Locate every blood parasite and identify its species.
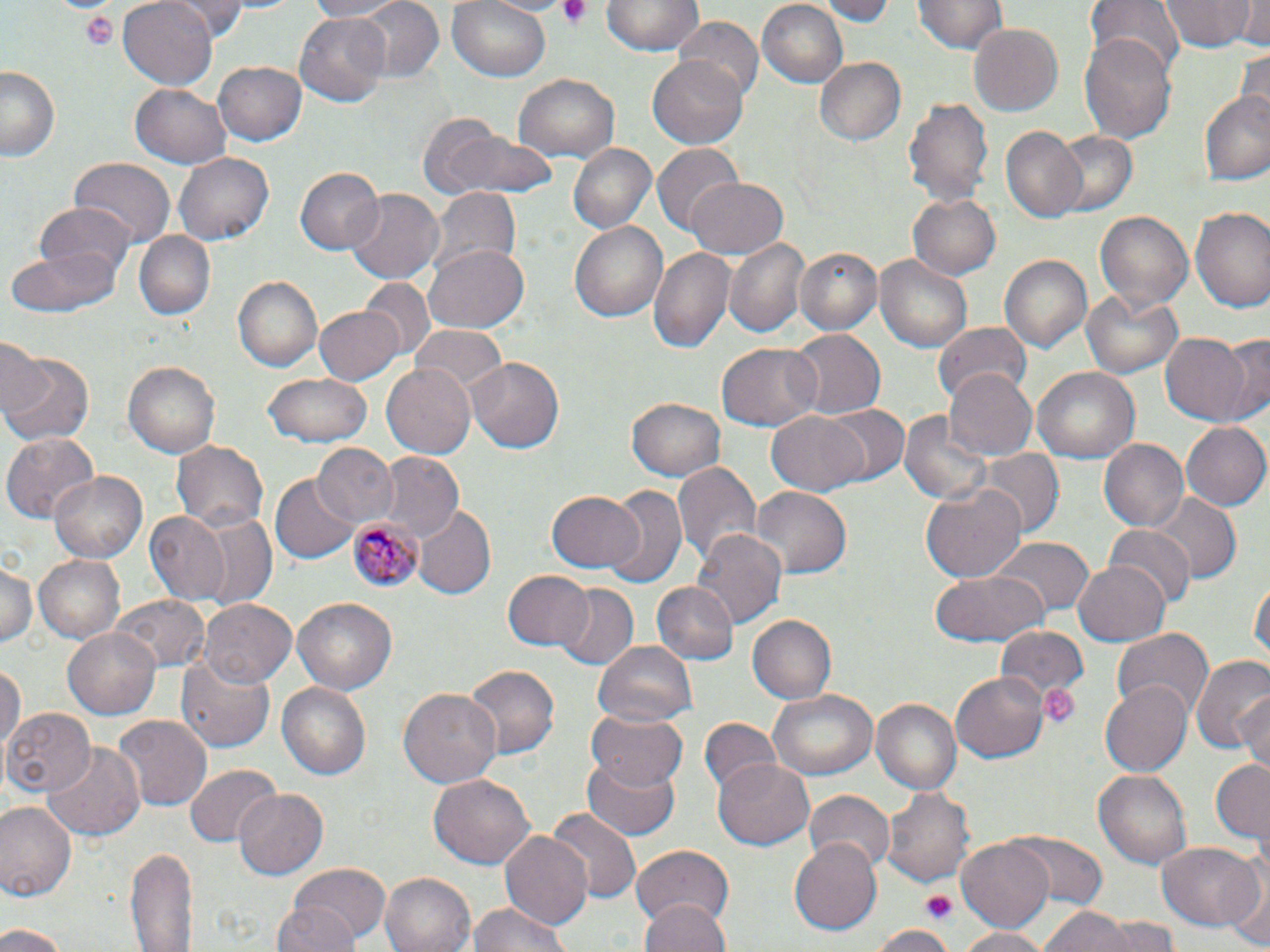

Approximate bounding boxes as named x1/y1/x2/y2 corners in pixels.
Plasmodium malariae-infected red blood cells: (x1=348, y1=516, x2=419, y2=592).
No Plasmodium falciparum, Plasmodium ovale, Plasmodium vivax, Babesia divergens, or Trypanosoma brucei observed.

{
  "slide_level_diagnosis": "Plasmodium malariae",
  "stain": "May-Grünwald-Giemsa",
  "modality": "light microscopy",
  "preparation": "thin blood film",
  "field_of_view": "single",
  "magnification": "1000x",
  "platelet_locations": "approximate bounding boxes as named x1/y1/x2/y2 corners in pixels: (x1=555, y1=0, x2=595, y2=29), (x1=79, y1=9, x2=119, y2=49), (x1=1039, y1=683, x2=1080, y2=730), (x1=920, y1=891, x2=958, y2=923)",
  "image_size": "1270×952 pixels",
  "uninfected_red_blood_cell_locations": "approximate bounding boxes as named x1/y1/x2/y2 corners in pixels: (x1=119, y1=0, x2=218, y2=89), (x1=171, y1=0, x2=256, y2=38), (x1=302, y1=0, x2=410, y2=21), (x1=346, y1=0, x2=446, y2=83), (x1=448, y1=0, x2=552, y2=82), (x1=484, y1=0, x2=573, y2=16), (x1=604, y1=0, x2=701, y2=55), (x1=815, y1=0, x2=896, y2=23), (x1=915, y1=0, x2=1006, y2=55), (x1=1085, y1=0, x2=1184, y2=79), (x1=1161, y1=0, x2=1258, y2=51), (x1=1235, y1=0, x2=1270, y2=47), (x1=755, y1=1, x2=849, y2=88), (x1=295, y1=12, x2=392, y2=106), (x1=674, y1=17, x2=763, y2=105), (x1=969, y1=22, x2=1064, y2=116), (x1=1083, y1=30, x2=1177, y2=146), (x1=1235, y1=46, x2=1270, y2=125), (x1=648, y1=55, x2=752, y2=150), (x1=813, y1=56, x2=909, y2=148), (x1=212, y1=61, x2=307, y2=146), (x1=2, y1=66, x2=62, y2=163), (x1=511, y1=74, x2=618, y2=163), (x1=131, y1=84, x2=232, y2=169), (x1=1200, y1=89, x2=1270, y2=185), (x1=903, y1=95, x2=993, y2=208), (x1=416, y1=114, x2=551, y2=202), (x1=999, y1=126, x2=1086, y2=220), (x1=1045, y1=130, x2=1138, y2=217), (x1=567, y1=142, x2=656, y2=233), (x1=651, y1=144, x2=743, y2=234), (x1=175, y1=152, x2=272, y2=245), (x1=70, y1=160, x2=174, y2=248), (x1=295, y1=165, x2=382, y2=255), (x1=684, y1=175, x2=787, y2=258), (x1=428, y1=189, x2=519, y2=281), (x1=345, y1=190, x2=442, y2=282), (x1=908, y1=194, x2=1001, y2=278), (x1=31, y1=204, x2=137, y2=283), (x1=1191, y1=206, x2=1270, y2=315), (x1=1093, y1=209, x2=1195, y2=316), (x1=570, y1=222, x2=665, y2=321), (x1=136, y1=232, x2=214, y2=321), (x1=724, y1=238, x2=811, y2=340), (x1=424, y1=243, x2=529, y2=335), (x1=648, y1=245, x2=736, y2=355), (x1=795, y1=247, x2=882, y2=337), (x1=4, y1=248, x2=120, y2=320), (x1=1000, y1=253, x2=1091, y2=354), (x1=876, y1=256, x2=972, y2=352), (x1=232, y1=276, x2=323, y2=373), (x1=362, y1=280, x2=433, y2=356), (x1=1082, y1=291, x2=1182, y2=377), (x1=312, y1=304, x2=404, y2=385), (x1=932, y1=320, x2=1034, y2=401), (x1=409, y1=326, x2=509, y2=397), (x1=787, y1=328, x2=882, y2=420), (x1=1161, y1=333, x2=1253, y2=425), (x1=1220, y1=335, x2=1270, y2=424), (x1=0, y1=336, x2=48, y2=422), (x1=717, y1=341, x2=822, y2=432), (x1=1, y1=349, x2=92, y2=446), (x1=467, y1=358, x2=565, y2=452), (x1=123, y1=361, x2=217, y2=459), (x1=383, y1=366, x2=476, y2=459), (x1=1033, y1=366, x2=1139, y2=463), (x1=944, y1=367, x2=1037, y2=458), (x1=264, y1=372, x2=374, y2=446), (x1=627, y1=396, x2=727, y2=480), (x1=821, y1=404, x2=909, y2=486), (x1=899, y1=407, x2=996, y2=508), (x1=766, y1=410, x2=870, y2=494), (x1=1180, y1=421, x2=1267, y2=511), (x1=4, y1=431, x2=102, y2=522), (x1=1100, y1=438, x2=1192, y2=532), (x1=172, y1=439, x2=268, y2=531), (x1=311, y1=443, x2=400, y2=526), (x1=979, y1=448, x2=1062, y2=535), (x1=376, y1=455, x2=463, y2=543), (x1=673, y1=459, x2=762, y2=568), (x1=52, y1=471, x2=147, y2=560), (x1=273, y1=475, x2=358, y2=563), (x1=921, y1=481, x2=1026, y2=583), (x1=601, y1=485, x2=688, y2=591), (x1=753, y1=486, x2=853, y2=576), (x1=547, y1=489, x2=644, y2=575), (x1=1148, y1=493, x2=1241, y2=582), (x1=412, y1=506, x2=495, y2=600), (x1=185, y1=511, x2=278, y2=611), (x1=144, y1=512, x2=228, y2=604), (x1=1104, y1=524, x2=1195, y2=609), (x1=691, y1=528, x2=786, y2=632), (x1=990, y1=538, x2=1093, y2=620), (x1=34, y1=553, x2=124, y2=642), (x1=1072, y1=558, x2=1170, y2=644), (x1=0, y1=562, x2=38, y2=651), (x1=931, y1=569, x2=1051, y2=646), (x1=503, y1=570, x2=595, y2=651), (x1=1251, y1=574, x2=1269, y2=668), (x1=650, y1=580, x2=736, y2=663), (x1=552, y1=583, x2=639, y2=673), (x1=112, y1=593, x2=209, y2=670), (x1=290, y1=597, x2=398, y2=698), (x1=199, y1=599, x2=296, y2=689), (x1=747, y1=613, x2=839, y2=704), (x1=994, y1=624, x2=1088, y2=711), (x1=63, y1=626, x2=163, y2=720), (x1=1112, y1=629, x2=1214, y2=717), (x1=595, y1=641, x2=697, y2=725), (x1=177, y1=656, x2=276, y2=752), (x1=1191, y1=656, x2=1270, y2=754), (x1=0, y1=663, x2=23, y2=757), (x1=463, y1=664, x2=560, y2=756), (x1=951, y1=675, x2=1047, y2=761), (x1=276, y1=680, x2=372, y2=781), (x1=1100, y1=681, x2=1192, y2=773), (x1=400, y1=687, x2=502, y2=790), (x1=769, y1=688, x2=878, y2=782), (x1=1238, y1=689, x2=1270, y2=776), (x1=869, y1=695, x2=961, y2=794), (x1=3, y1=707, x2=94, y2=796), (x1=587, y1=711, x2=690, y2=791), (x1=113, y1=715, x2=211, y2=811), (x1=697, y1=718, x2=781, y2=800), (x1=41, y1=740, x2=145, y2=845), (x1=583, y1=753, x2=681, y2=838), (x1=713, y1=758, x2=816, y2=849), (x1=1211, y1=758, x2=1269, y2=848), (x1=187, y1=764, x2=279, y2=848), (x1=1093, y1=768, x2=1195, y2=868), (x1=427, y1=774, x2=536, y2=869), (x1=881, y1=783, x2=975, y2=889), (x1=233, y1=787, x2=328, y2=880), (x1=807, y1=789, x2=894, y2=872), (x1=0, y1=799, x2=78, y2=900), (x1=546, y1=807, x2=642, y2=905), (x1=1003, y1=830, x2=1108, y2=908), (x1=499, y1=832, x2=593, y2=930), (x1=958, y1=837, x2=1054, y2=933), (x1=788, y1=838, x2=881, y2=935), (x1=1156, y1=842, x2=1264, y2=931), (x1=631, y1=843, x2=736, y2=931), (x1=127, y1=845, x2=194, y2=952), (x1=1222, y1=861, x2=1269, y2=950), (x1=288, y1=864, x2=389, y2=944), (x1=381, y1=872, x2=477, y2=952), (x1=643, y1=896, x2=730, y2=952), (x1=468, y1=898, x2=573, y2=952), (x1=272, y1=900, x2=363, y2=952), (x1=1038, y1=906, x2=1135, y2=952), (x1=1097, y1=917, x2=1182, y2=950), (x1=0, y1=923, x2=68, y2=952), (x1=870, y1=925, x2=957, y2=952), (x1=956, y1=927, x2=1051, y2=952)"
}